Identify the parasite.
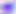
This is Toxoplasma gondii.

modality = micrograph
magnification = 400x